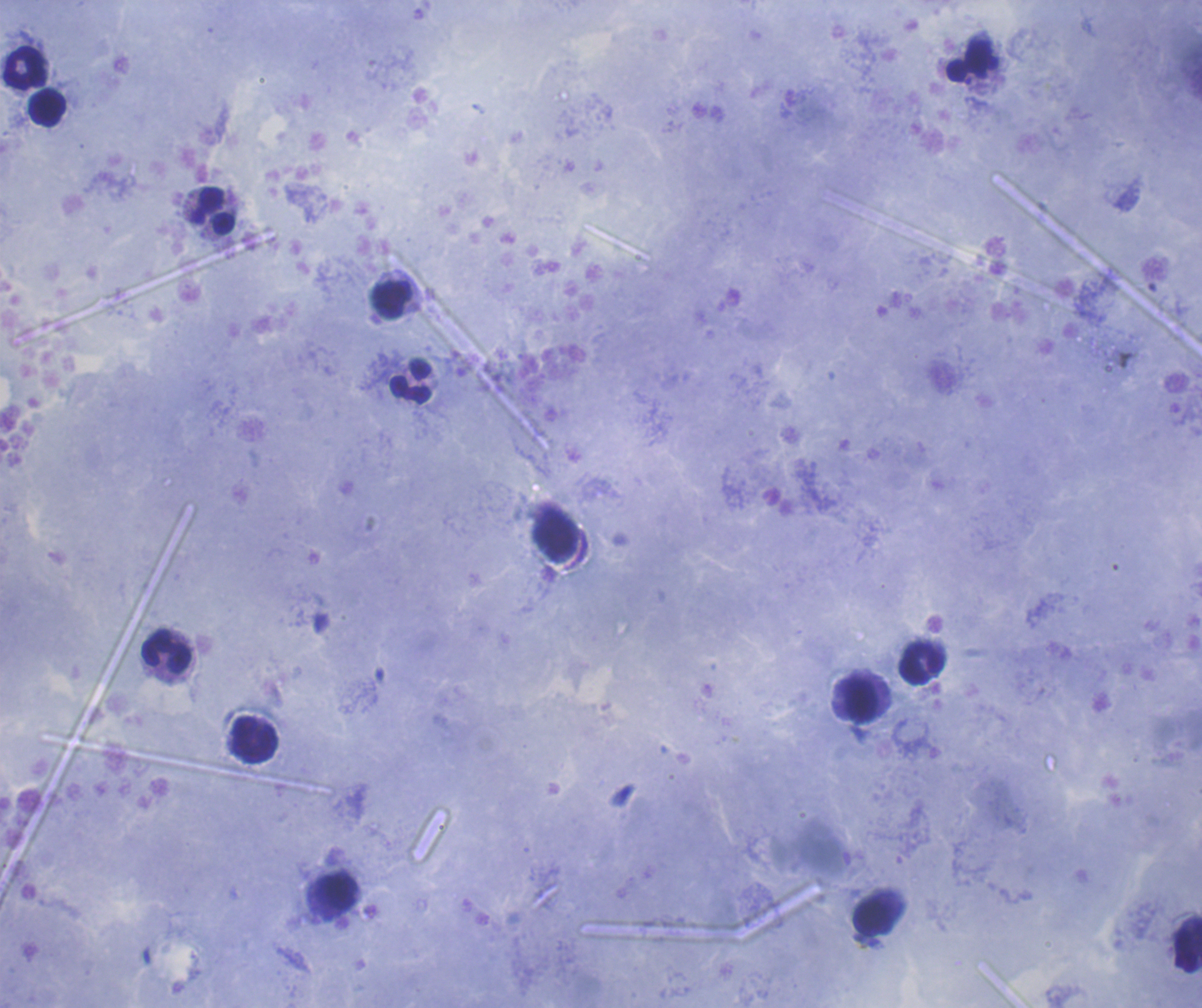
Approximate centers as [x, y] in pixels. Leukocyte locations: [969, 61], [25, 68], [47, 108], [213, 210], [392, 300], [411, 381], [556, 535], [167, 652], [923, 663], [862, 699], [254, 741], [337, 892], [873, 917], [1187, 945]. Previously used in an actual diagnosis. Single field of view. Result: no malaria parasites seen. Thick smear of blood. Image is 1202×1008 pixels. Coloration quality: good. 100x magnification. Background quality: satisfactory. Romanowsky stain.